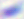

{
  "magnification": "400x",
  "identification": "Toxoplasma gondii",
  "modality": "micrograph"
}